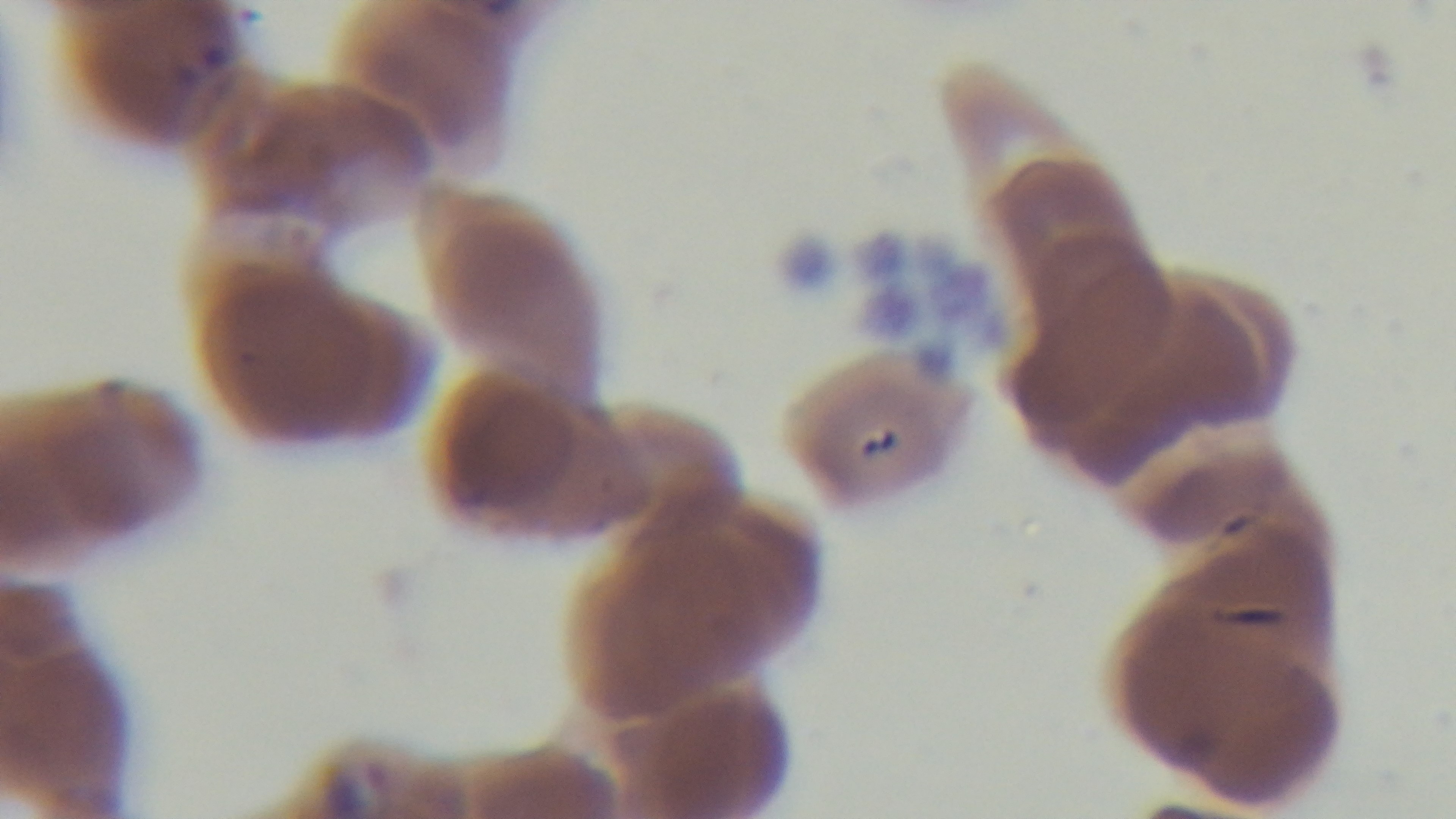

Summary:
  - Preparation: thin blood film
  - Stain: Giemsa
  - Capture: mounted 4K digital camera
  - Objective: 100x oil immersion
  - Modality: light microscopy
  - Field of view: single
  - Malaria status: positive